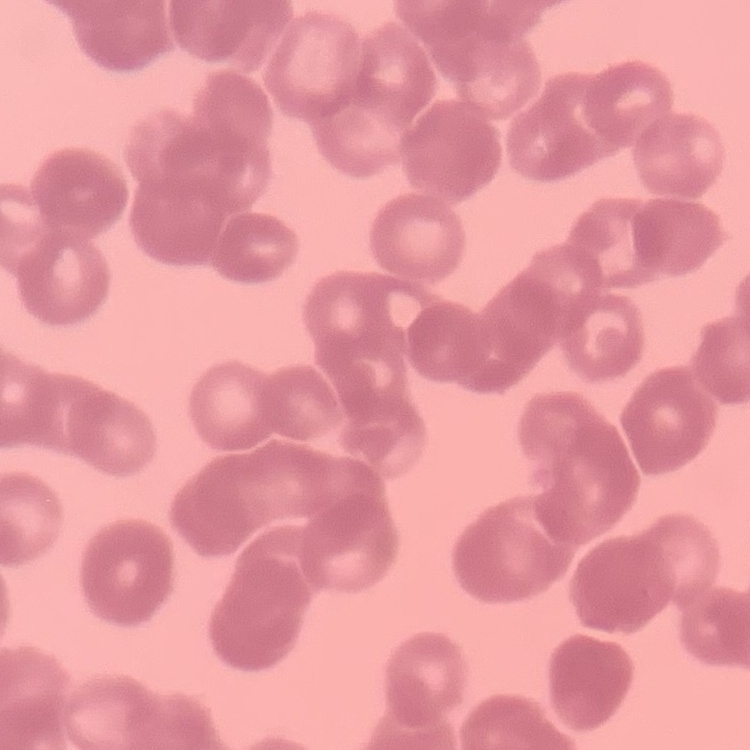

erythrocyte morphology = rouleaux formation
preparation = thin peripheral smear
image type = square crop of a larger photomicrograph
stain = Field's or Giemsa